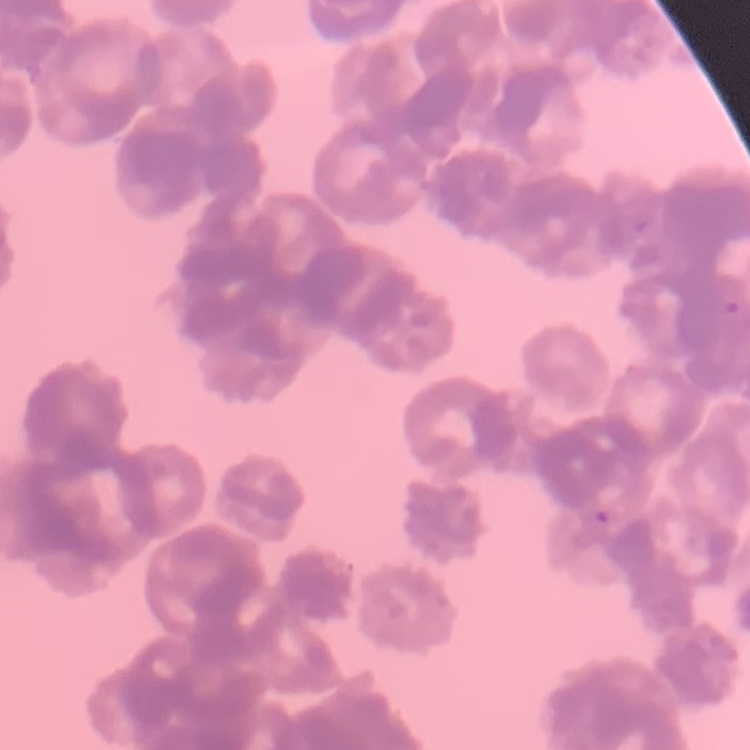

The red blood cells exhibit rouleaux formation. Thin peripheral smear. Stained with either Field's or Giemsa. Square crop of a larger photomicrograph.